Locate every uninfected red blood cell.
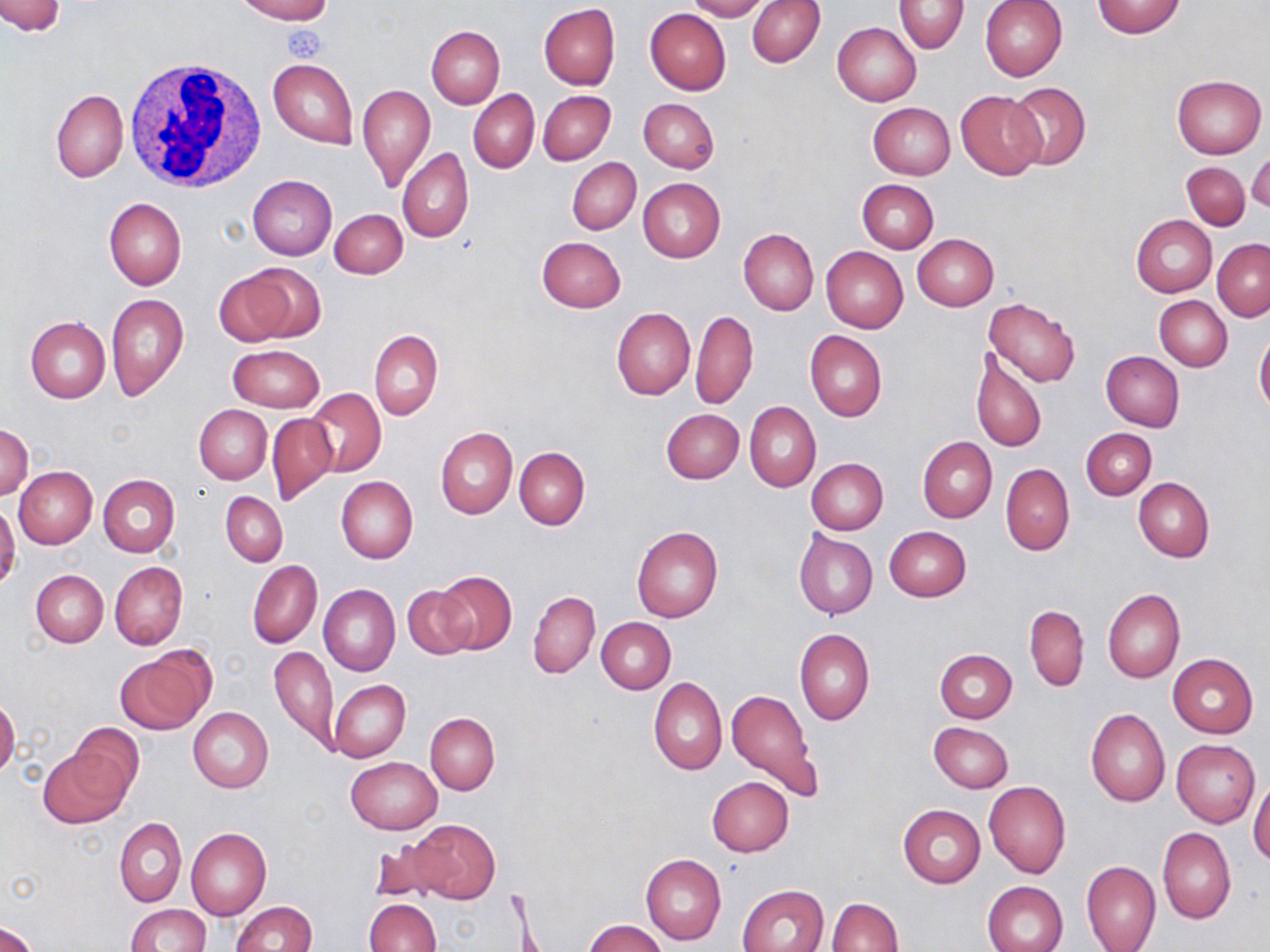
Approximate bounding boxes as named x1/y1/x2/y2 corners in pixels.
Uninfected red blood cells: (x1=0, y1=0, x2=64, y2=37), (x1=236, y1=0, x2=332, y2=24), (x1=684, y1=0, x2=768, y2=20), (x1=980, y1=0, x2=1067, y2=81), (x1=748, y1=1, x2=825, y2=67), (x1=894, y1=1, x2=969, y2=54), (x1=1092, y1=1, x2=1186, y2=38), (x1=539, y1=3, x2=620, y2=91), (x1=645, y1=8, x2=731, y2=96), (x1=832, y1=22, x2=921, y2=105), (x1=426, y1=26, x2=504, y2=107), (x1=269, y1=58, x2=357, y2=150), (x1=1172, y1=74, x2=1266, y2=158), (x1=1006, y1=82, x2=1090, y2=169), (x1=357, y1=84, x2=434, y2=192), (x1=51, y1=88, x2=127, y2=182), (x1=469, y1=89, x2=539, y2=173), (x1=538, y1=90, x2=615, y2=164), (x1=955, y1=90, x2=1046, y2=179), (x1=639, y1=98, x2=719, y2=174), (x1=868, y1=102, x2=955, y2=179), (x1=398, y1=147, x2=474, y2=244), (x1=1247, y1=153, x2=1270, y2=212), (x1=568, y1=157, x2=641, y2=234), (x1=1181, y1=161, x2=1250, y2=230), (x1=247, y1=175, x2=337, y2=259), (x1=638, y1=178, x2=725, y2=262), (x1=857, y1=180, x2=937, y2=253), (x1=105, y1=198, x2=186, y2=290), (x1=331, y1=208, x2=408, y2=279), (x1=1131, y1=215, x2=1217, y2=297), (x1=738, y1=228, x2=819, y2=315), (x1=912, y1=235, x2=998, y2=311), (x1=537, y1=236, x2=625, y2=312), (x1=1213, y1=238, x2=1270, y2=321), (x1=821, y1=246, x2=907, y2=333), (x1=214, y1=266, x2=319, y2=348), (x1=105, y1=293, x2=189, y2=400), (x1=1155, y1=295, x2=1233, y2=371), (x1=983, y1=298, x2=1082, y2=387), (x1=611, y1=306, x2=694, y2=400), (x1=691, y1=309, x2=758, y2=410), (x1=25, y1=317, x2=110, y2=403), (x1=369, y1=329, x2=443, y2=421), (x1=805, y1=330, x2=887, y2=422), (x1=1254, y1=332, x2=1270, y2=416), (x1=228, y1=345, x2=324, y2=411), (x1=969, y1=348, x2=1047, y2=455), (x1=1101, y1=352, x2=1184, y2=431), (x1=1089, y1=354, x2=1166, y2=500), (x1=306, y1=388, x2=386, y2=476), (x1=745, y1=401, x2=821, y2=493), (x1=194, y1=405, x2=272, y2=483), (x1=661, y1=409, x2=743, y2=484), (x1=266, y1=413, x2=337, y2=505), (x1=0, y1=424, x2=33, y2=502), (x1=435, y1=427, x2=517, y2=519), (x1=1081, y1=428, x2=1156, y2=500), (x1=918, y1=437, x2=996, y2=523), (x1=514, y1=446, x2=590, y2=529), (x1=806, y1=458, x2=887, y2=534), (x1=1001, y1=463, x2=1074, y2=555), (x1=14, y1=466, x2=97, y2=548), (x1=99, y1=475, x2=179, y2=557), (x1=335, y1=476, x2=418, y2=563), (x1=1133, y1=477, x2=1214, y2=562), (x1=222, y1=492, x2=288, y2=566), (x1=0, y1=503, x2=20, y2=590), (x1=631, y1=526, x2=724, y2=623), (x1=884, y1=526, x2=970, y2=602), (x1=794, y1=530, x2=878, y2=619), (x1=247, y1=560, x2=322, y2=649), (x1=109, y1=561, x2=187, y2=651), (x1=31, y1=570, x2=107, y2=647), (x1=433, y1=571, x2=517, y2=655), (x1=319, y1=584, x2=400, y2=676), (x1=402, y1=586, x2=476, y2=659), (x1=1102, y1=589, x2=1185, y2=683), (x1=529, y1=591, x2=600, y2=677), (x1=1024, y1=604, x2=1088, y2=692), (x1=597, y1=618, x2=675, y2=693), (x1=795, y1=627, x2=875, y2=724), (x1=115, y1=647, x2=213, y2=735), (x1=269, y1=647, x2=338, y2=752), (x1=935, y1=649, x2=1016, y2=723), (x1=1168, y1=654, x2=1258, y2=737), (x1=648, y1=677, x2=727, y2=775), (x1=329, y1=679, x2=410, y2=763), (x1=725, y1=688, x2=823, y2=803), (x1=0, y1=697, x2=20, y2=780), (x1=187, y1=707, x2=273, y2=793), (x1=1086, y1=708, x2=1170, y2=807), (x1=426, y1=713, x2=500, y2=794), (x1=72, y1=722, x2=144, y2=803), (x1=930, y1=722, x2=1014, y2=792), (x1=1171, y1=739, x2=1260, y2=827), (x1=38, y1=747, x2=133, y2=829), (x1=346, y1=756, x2=442, y2=833), (x1=1249, y1=774, x2=1270, y2=865), (x1=707, y1=777, x2=794, y2=857), (x1=984, y1=781, x2=1070, y2=878), (x1=899, y1=805, x2=984, y2=887), (x1=115, y1=817, x2=187, y2=907), (x1=403, y1=818, x2=500, y2=904), (x1=186, y1=826, x2=270, y2=920), (x1=1158, y1=828, x2=1235, y2=924), (x1=370, y1=842, x2=441, y2=903), (x1=640, y1=854, x2=727, y2=946), (x1=1080, y1=860, x2=1160, y2=952), (x1=983, y1=881, x2=1068, y2=952), (x1=737, y1=884, x2=828, y2=952), (x1=828, y1=897, x2=901, y2=951), (x1=365, y1=898, x2=440, y2=952), (x1=231, y1=900, x2=317, y2=952), (x1=124, y1=904, x2=210, y2=951), (x1=583, y1=918, x2=668, y2=952), (x1=0, y1=922, x2=38, y2=952).

Platelet locations: (x1=284, y1=25, x2=326, y2=62). White blood cell locations: (x1=124, y1=58, x2=266, y2=190). Slide-level diagnosis: no evidence of blood parasites. Captured at 1000x magnification. Optical microscopy. Thin blood film. Image is 1270×952 pixels. May-Grünwald-Giemsa-stained preparation. Single field of view.